Assess this cell for malaria.
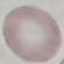
It is uninfected.

preparation = thin blood film
image type = automatically extracted cell patch, resized to 64 × 64 pixels
capture = smartphone camera at the microscope eyepiece
stain = Giemsa